Describe the morphology of the red blood cells.
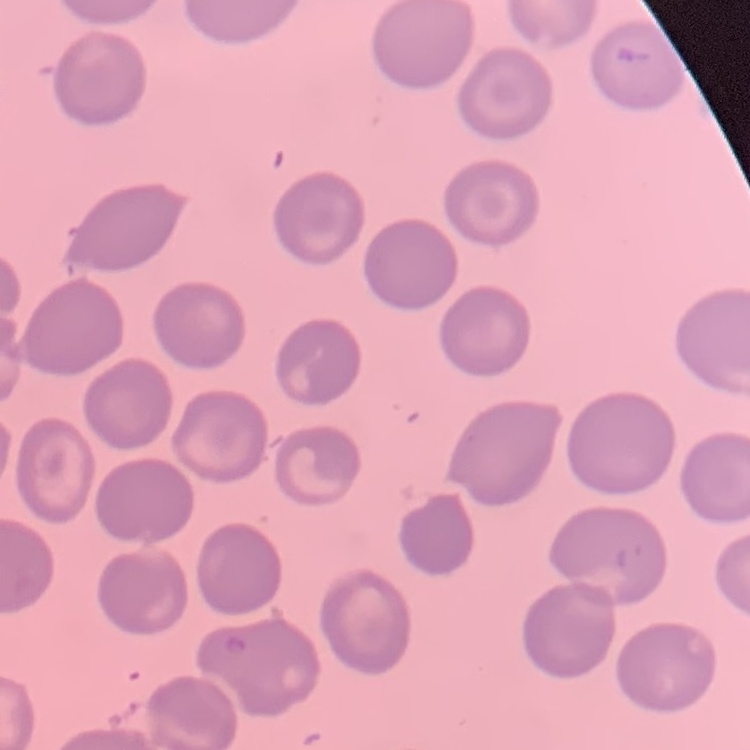

No rouleaux formation.

{
  "stain": "Field's or Giemsa",
  "preparation": "thin peripheral smear",
  "image_type": "square crop of a larger photomicrograph"
}